Give the preparation type.
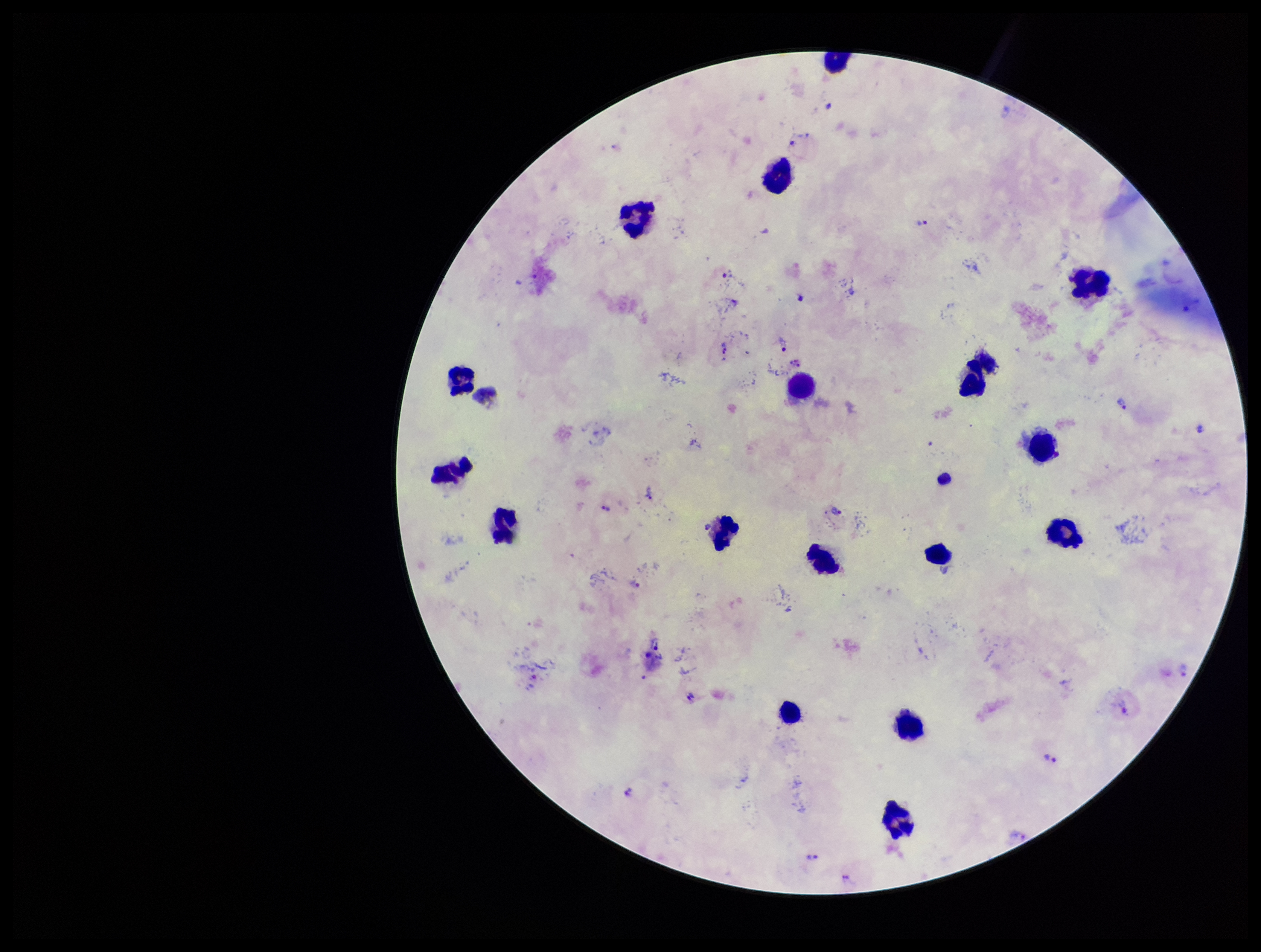

Thick.

Plasmodium parasites = detected
species reported for this patient = Plasmodium vivax
stain = Giemsa
capture = smartphone photograph through the microscope eyepiece
parasite count = 25
field of view = one from this slide
leukocyte count = 19
patient malaria status = positive
image size = 1261×952 pixels